Name the parasite shown.
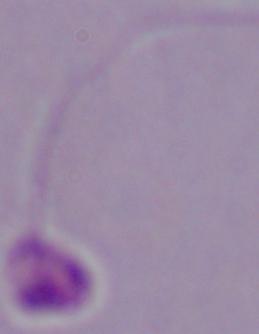
This is Leishmania.

modality = micrograph
magnification = 1000x